Assess this cell for malaria.
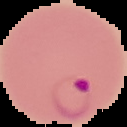

It is parasitized.

image type = segmented cell region with the area outside set to black
image size = 127×127 pixels
preparation = thin blood smear